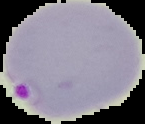

Summary:
  - Preparation: thin blood film
  - Image type: cell region segmented out of the field of view; surrounding area masked to black
  - Image size: 145×124 pixels
  - Malaria status: parasitized